Comment on the morphology of the red blood cells.
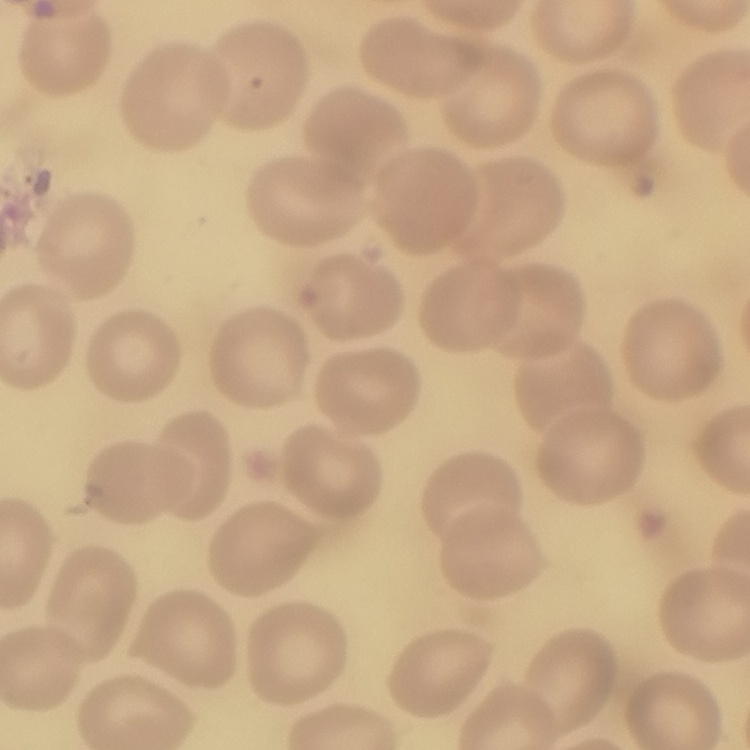
No rouleaux formation.

Field's or Giemsa stain. Square crop of a larger photomicrograph. Thin blood smear.